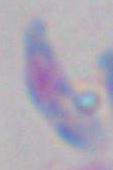

identification = Toxoplasma gondii
modality = photomicrograph
magnification = 1000x